Outline each blood parasite and name the species.
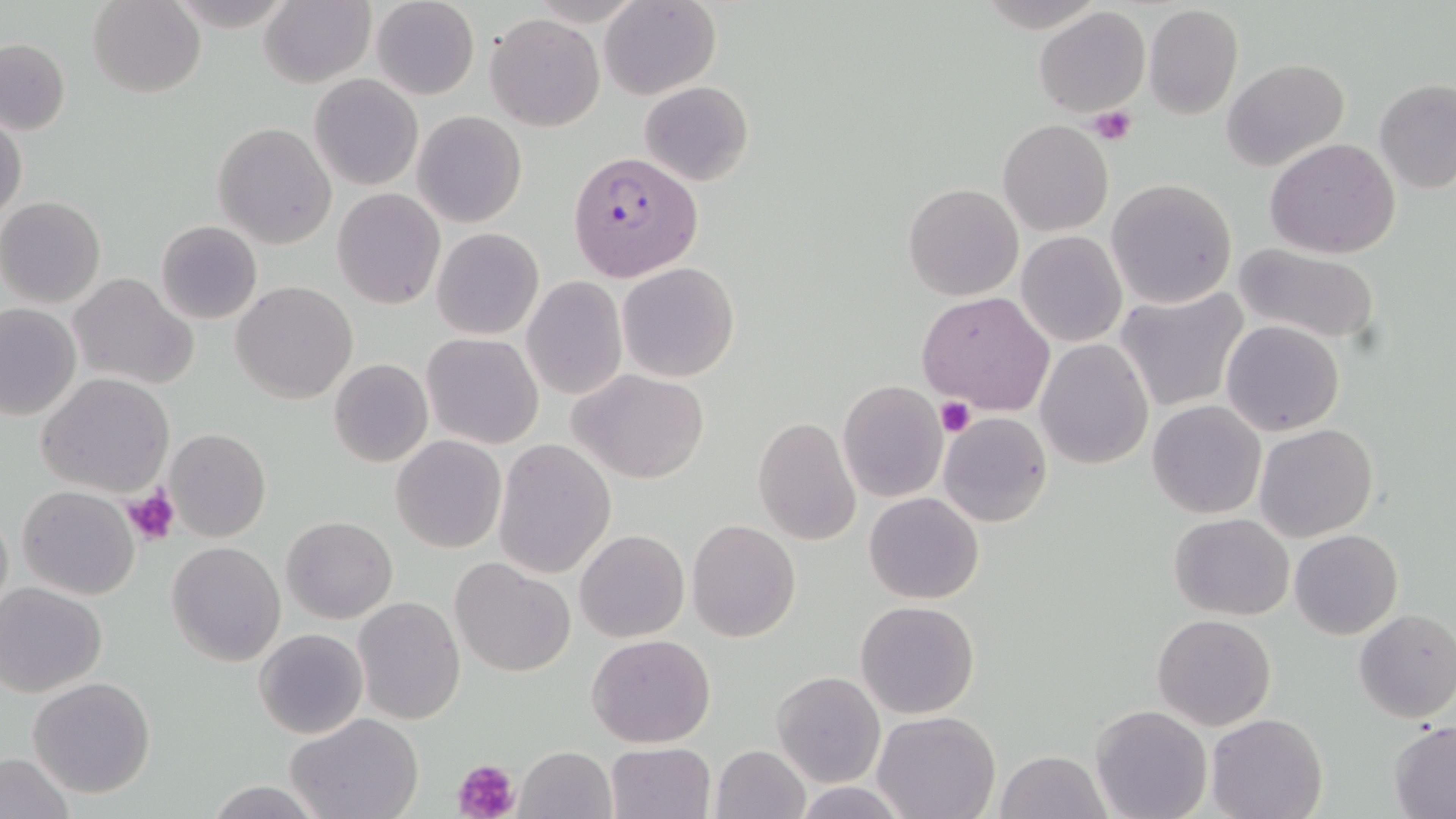

Approximate bounding boxes as (x1,y1)-(x2,y2) corner pairs in pixels.
Plasmodium falciparum-infected red blood cells: (567,150)-(702,283).
No Plasmodium ovale, Plasmodium malariae, Plasmodium vivax, Babesia divergens, or Trypanosoma brucei observed.

Summary:
  - Uninfected red blood cell locations: (88,0)-(204,98), (260,0)-(375,88), (371,0)-(478,99), (600,0)-(721,99), (1143,5)-(1243,120), (1034,7)-(1151,118), (486,13)-(604,131), (0,37)-(70,135), (1221,58)-(1350,172), (309,74)-(423,190), (1374,79)-(1456,195), (639,81)-(754,186), (413,111)-(527,227), (1,114)-(26,221), (999,118)-(1113,235), (213,122)-(337,249), (1264,138)-(1403,258), (1106,178)-(1237,308), (902,182)-(1023,301), (333,188)-(446,310), (0,197)-(106,307), (155,220)-(262,324), (431,227)-(544,341), (1016,230)-(1127,347), (469,241)-(590,382), (1230,243)-(1384,347), (616,261)-(740,383), (68,273)-(198,390), (522,277)-(626,400), (232,281)-(358,404), (1115,289)-(1249,415), (917,292)-(1054,414), (0,302)-(81,420), (1222,321)-(1345,436), (421,333)-(544,448), (1036,338)-(1154,469), (329,358)-(433,468), (569,368)-(710,484), (38,373)-(176,497), (837,382)-(949,503), (1148,401)-(1266,518), (938,411)-(1052,527), (753,415)-(862,544), (1254,424)-(1379,542), (165,427)-(271,543), (391,435)-(506,553), (493,438)-(616,578), (17,486)-(141,599), (865,491)-(983,604), (1169,512)-(1295,620), (281,516)-(397,622), (688,520)-(801,642), (575,529)-(689,642), (1289,530)-(1402,640), (167,542)-(284,664), (450,557)-(576,677), (0,582)-(109,697), (353,596)-(466,725), (855,600)-(981,719), (1353,608)-(1456,723), (1153,613)-(1276,730), (253,628)-(368,740), (587,634)-(715,748), (772,671)-(886,787), (28,676)-(156,798), (1090,704)-(1213,819), (872,710)-(1001,819), (286,713)-(425,819), (1206,713)-(1328,819), (1388,721)-(1456,818), (604,742)-(715,819), (709,744)-(811,819), (516,746)-(617,819), (994,749)-(1111,819), (0,752)-(76,819), (205,781)-(324,817), (790,781)-(913,818)
  - Platelet locations: (1087,107)-(1137,146), (936,398)-(976,438), (122,485)-(181,545), (455,757)-(521,819)
  - Slide-level diagnosis: Plasmodium falciparum
  - Stain: May-Grünwald-Giemsa
  - Preparation: thin blood film
  - Magnification: 1000x
  - Modality: light microscopy
  - Image size: 1456×819 pixels
  - Field of view: one of a larger specimen